Identify the cell.
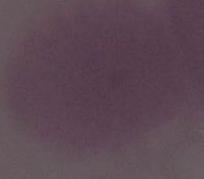

This is an erythrocyte.

modality = micrograph
magnification = 1000x